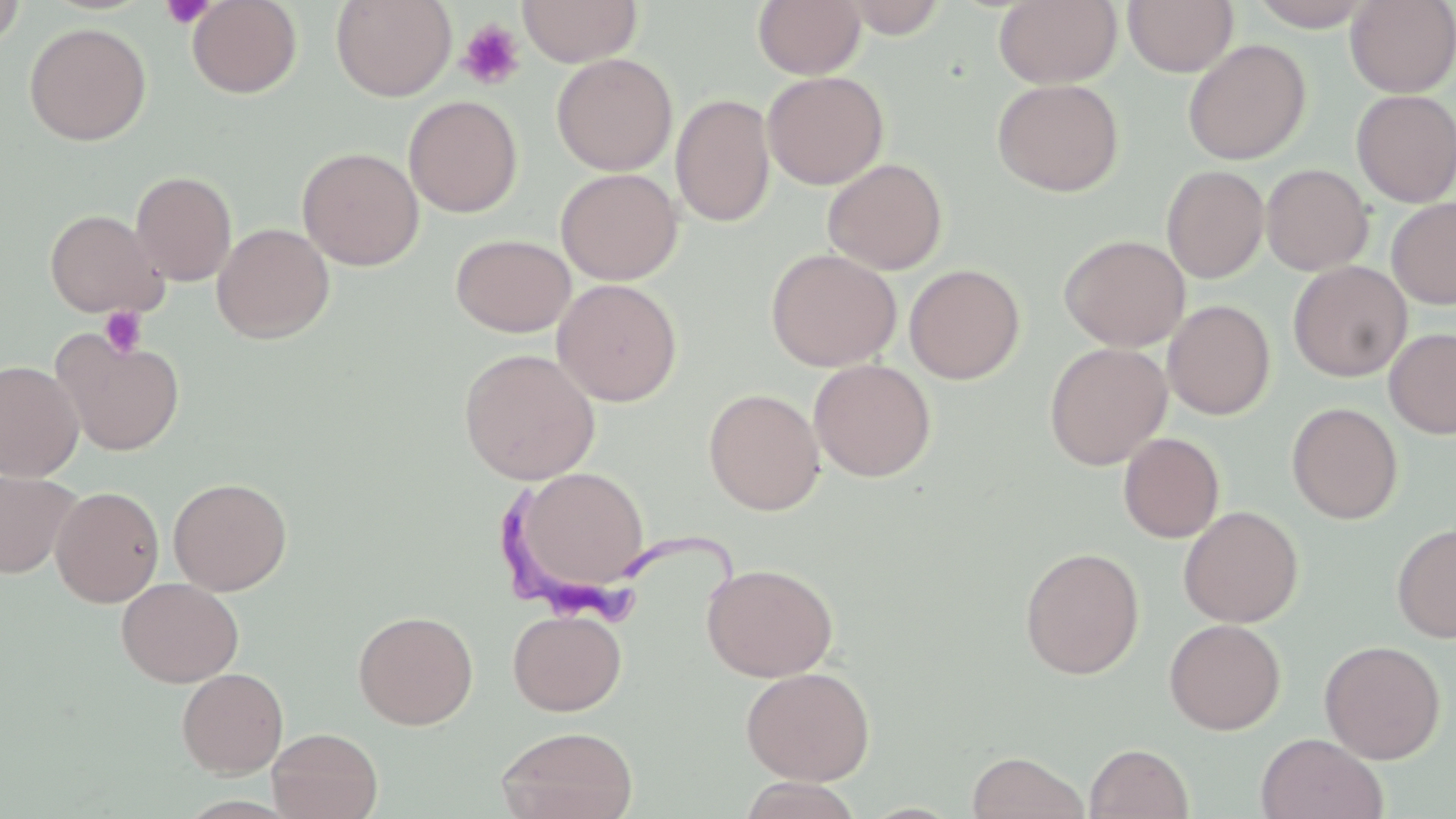

slide-level diagnosis = Trypanosoma brucei
modality = light microscopy
uninfected red blood cell locations = approximate bounding boxes as (x1,y1)-(x2,y2) corner pairs in pixels: (0,0)-(27,50), (186,0)-(302,98), (331,0)-(456,101), (518,0)-(642,67), (753,0)-(866,79), (838,0)-(949,38), (995,0)-(1121,88), (1123,0)-(1238,76), (1248,0)-(1376,30), (1345,1)-(1456,97), (23,22)-(151,146), (1183,39)-(1311,165), (551,53)-(678,176), (762,71)-(889,189), (992,78)-(1124,197), (1351,89)-(1456,208), (670,94)-(776,227), (403,95)-(523,218), (297,147)-(424,271), (823,158)-(948,274), (1261,163)-(1374,276), (1161,165)-(1270,284), (555,168)-(683,285), (131,170)-(237,286), (1387,198)-(1456,309), (45,209)-(166,318), (212,223)-(335,344), (451,234)-(576,338), (1059,234)-(1190,352), (765,248)-(902,372), (1288,261)-(1412,381), (904,263)-(1026,384), (552,278)-(682,406), (1162,300)-(1275,420), (1384,328)-(1456,438), (52,330)-(185,456), (1044,342)-(1172,470), (459,347)-(600,484), (809,358)-(936,482), (0,359)-(84,482), (703,387)-(825,515), (1287,402)-(1403,524), (1118,432)-(1225,543), (513,466)-(650,593), (0,470)-(82,578), (168,477)-(292,596), (50,485)-(165,607), (1178,506)-(1303,627), (1392,522)-(1456,644), (1020,547)-(1145,679), (701,562)-(839,682), (116,577)-(244,687), (508,608)-(627,716), (352,609)-(478,729), (1164,618)-(1286,734), (1319,640)-(1445,764), (740,665)-(876,785), (177,668)-(288,777), (496,725)-(638,819), (267,727)-(383,819), (1256,733)-(1388,819), (1085,743)-(1194,819), (966,750)-(1089,819)
field of view = one of a larger specimen
platelet locations = approximate bounding boxes as (x1,y1)-(x2,y2) corner pairs in pixels: (160,0)-(216,30), (456,19)-(526,90), (100,306)-(148,358)
magnification = 1000x
stain = May-Grünwald-Giemsa
Trypanosoma brucei locations = approximate bounding boxes as (x1,y1)-(x2,y2) corner pairs in pixels: (493,479)-(749,628)
image size = 1456×819 pixels
preparation = thin blood smear